Report the malaria status of this cell.
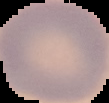

It is uninfected.

Summary:
  - Preparation: thin blood film
  - Image type: cell region segmented out of the field of view; surrounding area masked to black
  - Image size: 109×103 pixels